Find each parasitized red blood cell.
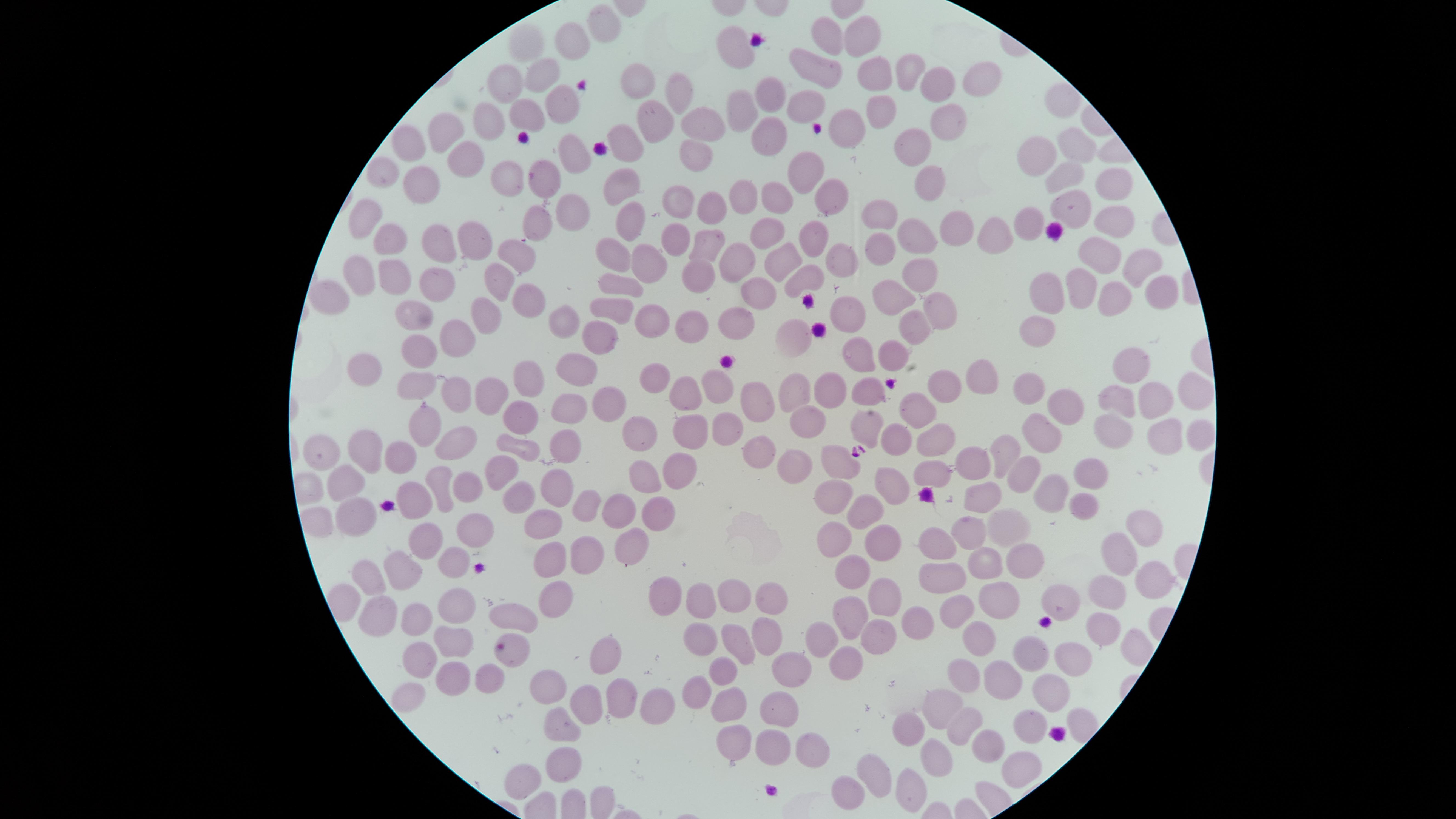

No parasitized red blood cells identified.

Approximate marker points as [x, y] in pixels. Uninfected red blood cells: [600, 24], [863, 35], [529, 36], [830, 38], [573, 43], [734, 45], [816, 66], [907, 69], [539, 71], [874, 73], [981, 77], [503, 81], [938, 83], [638, 84], [764, 90], [678, 96], [554, 106], [810, 106], [878, 106], [739, 111], [525, 117], [485, 119], [945, 119], [655, 125], [707, 125], [761, 132], [443, 134], [845, 134], [410, 143], [630, 143], [1071, 144], [912, 147], [690, 153], [463, 154], [1035, 154], [568, 156], [806, 167], [385, 172], [505, 174], [1062, 178], [540, 181], [931, 182], [416, 183], [624, 186], [1115, 187], [741, 193], [777, 198], [821, 198], [673, 199], [712, 202], [1068, 210], [879, 213], [568, 215], [370, 217], [630, 222], [1117, 222], [1028, 225], [532, 229], [771, 229], [956, 230], [993, 234], [912, 235], [463, 236], [392, 237], [682, 240], [814, 241], [704, 242], [434, 246], [878, 246], [610, 249], [515, 254], [1098, 257], [643, 258], [731, 259], [1138, 259], [778, 261], [696, 265], [841, 266], [357, 271], [920, 273], [391, 277], [799, 278], [498, 280], [434, 283], [1079, 283], [628, 285], [1049, 288], [1160, 288], [330, 295], [897, 295], [745, 298], [1108, 299], [530, 300], [843, 306], [487, 309], [614, 310], [936, 310], [415, 316], [650, 322], [729, 324], [564, 327], [914, 327], [685, 328], [1043, 329], [599, 333], [796, 335], [457, 337], [418, 348], [857, 352], [892, 353], [372, 368], [583, 368], [1134, 371], [653, 372], [985, 374], [532, 375], [717, 377], [416, 381], [864, 386], [1023, 388], [946, 389], [686, 391], [1191, 392], [454, 394], [792, 394], [825, 394], [491, 395], [1114, 398], [757, 402], [610, 405], [1151, 405], [918, 406], [1064, 407], [566, 413], [525, 420], [806, 420], [868, 422], [424, 423], [1118, 425], [1046, 427], [690, 432], [723, 432], [642, 436], [896, 436], [1160, 436], [558, 442], [933, 443], [457, 444], [519, 444], [398, 450], [755, 450], [363, 454], [1007, 454], [322, 456], [837, 464], [499, 467], [969, 467], [790, 468], [1017, 469], [642, 470], [1093, 471], [931, 472], [681, 474], [466, 481], [342, 485], [439, 485], [893, 485], [1047, 485], [554, 488], [982, 494], [520, 496], [833, 498], [412, 501], [1078, 501], [619, 509], [861, 511], [659, 512], [583, 513], [352, 522], [544, 522], [1007, 526], [1138, 527], [470, 529], [424, 534], [965, 536], [832, 539], [631, 540], [874, 542], [934, 547], [1117, 553], [581, 554], [1021, 557], [551, 560], [457, 564], [986, 564], [850, 568], [397, 570], [947, 575], [367, 578], [1149, 579], [877, 589], [662, 590], [1106, 593], [993, 597], [1059, 597], [551, 598], [729, 598], [763, 599], [696, 603], [451, 606], [850, 609], [953, 611], [375, 615], [512, 615], [414, 617], [917, 619], [1098, 624], [760, 634], [817, 636], [871, 637], [696, 639], [449, 641], [978, 644], [736, 645], [511, 650], [601, 653], [1029, 654], [417, 657], [1076, 659], [837, 660], [792, 664], [965, 671], [716, 673], [483, 674], [450, 676], [1002, 680], [549, 686], [1049, 686], [697, 690], [586, 698], [623, 698], [724, 701], [943, 704], [773, 706], [657, 710], [1026, 723], [558, 726], [958, 727], [909, 728], [770, 742], [726, 745], [804, 745], [984, 745], [935, 759], [1014, 766], [561, 768], [874, 774], [523, 780], [904, 789], [844, 791]. The visible region is circular. Smartphone photograph through the microscope eyepiece. Thin smear of blood. Giemsa-stained preparation. Image is 1456×819 pixels. Single field of view.